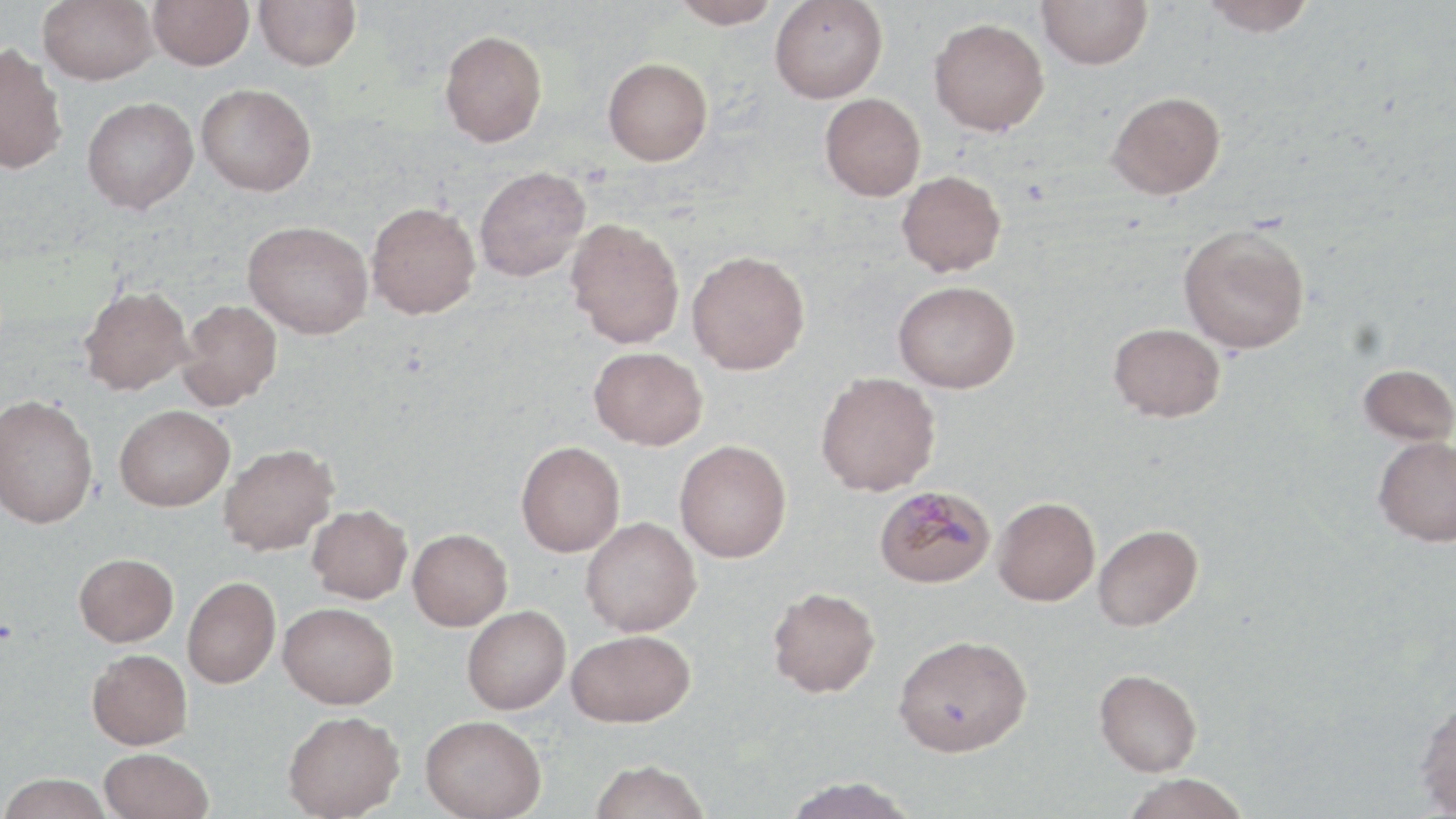

slide_level_diagnosis: Plasmodium malariae
preparation: thin blood smear
image_size: 1456×819 pixels
modality: light microscopy
plasmodium_malariae_infected_red_blood_cell_locations: 'approximate bounding boxes as named x1/y1/x2/y2 corners in pixels: (x1=875, y1=486, x2=997, y2=588)'
uninfected_red_blood_cell_locations: 'approximate bounding boxes as named x1/y1/x2/y2 corners in pixels: (x1=38, y1=0, x2=158, y2=85), (x1=148, y1=0, x2=253, y2=70), (x1=253, y1=0, x2=361, y2=71), (x1=671, y1=0, x2=780, y2=28), (x1=1037, y1=0, x2=1153, y2=70), (x1=1200, y1=0, x2=1317, y2=36), (x1=769, y1=1, x2=888, y2=103), (x1=929, y1=18, x2=1049, y2=136), (x1=440, y1=30, x2=547, y2=147), (x1=0, y1=43, x2=67, y2=175), (x1=602, y1=57, x2=713, y2=166), (x1=196, y1=83, x2=316, y2=196), (x1=1107, y1=91, x2=1225, y2=199), (x1=820, y1=92, x2=926, y2=200), (x1=82, y1=97, x2=198, y2=214), (x1=474, y1=166, x2=591, y2=281), (x1=897, y1=170, x2=1006, y2=277), (x1=366, y1=202, x2=480, y2=319), (x1=566, y1=219, x2=685, y2=348), (x1=243, y1=220, x2=373, y2=339), (x1=1178, y1=223, x2=1310, y2=354), (x1=687, y1=250, x2=810, y2=374), (x1=893, y1=280, x2=1020, y2=393), (x1=78, y1=285, x2=193, y2=395), (x1=178, y1=299, x2=282, y2=410), (x1=1109, y1=323, x2=1225, y2=422), (x1=589, y1=346, x2=707, y2=450), (x1=1358, y1=363, x2=1456, y2=446), (x1=815, y1=372, x2=941, y2=496), (x1=0, y1=394, x2=98, y2=528), (x1=114, y1=405, x2=234, y2=510), (x1=1373, y1=435, x2=1456, y2=546), (x1=675, y1=440, x2=792, y2=562), (x1=516, y1=441, x2=625, y2=557), (x1=218, y1=443, x2=338, y2=556), (x1=993, y1=497, x2=1100, y2=605), (x1=307, y1=505, x2=412, y2=604), (x1=581, y1=517, x2=701, y2=636), (x1=1092, y1=524, x2=1203, y2=631), (x1=408, y1=528, x2=512, y2=630), (x1=74, y1=553, x2=178, y2=647), (x1=183, y1=576, x2=280, y2=688), (x1=767, y1=586, x2=880, y2=697), (x1=279, y1=602, x2=398, y2=708), (x1=462, y1=606, x2=571, y2=714), (x1=566, y1=629, x2=695, y2=727), (x1=893, y1=634, x2=1032, y2=757), (x1=87, y1=649, x2=192, y2=749), (x1=1094, y1=669, x2=1202, y2=776), (x1=1414, y1=699, x2=1456, y2=817), (x1=282, y1=711, x2=405, y2=818), (x1=421, y1=714, x2=546, y2=819), (x1=99, y1=748, x2=213, y2=819), (x1=588, y1=758, x2=711, y2=819), (x1=0, y1=773, x2=113, y2=818), (x1=1121, y1=774, x2=1250, y2=819), (x1=780, y1=776, x2=919, y2=819)'
magnification: 1000x
stain: May-Grünwald-Giemsa
field_of_view: single